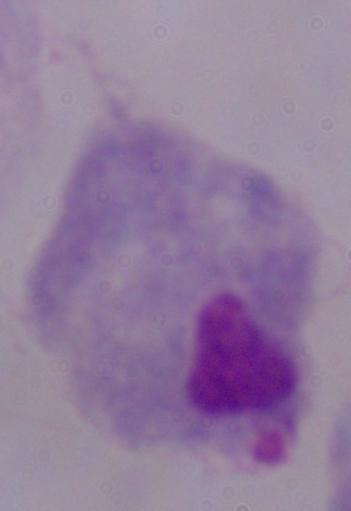 Photomicrograph. 1000x magnification. A trichomonad is seen.